Locate the cells, classifying each as a parasitized red blood cell, an uninfected red blood cell, or a white blood cell.
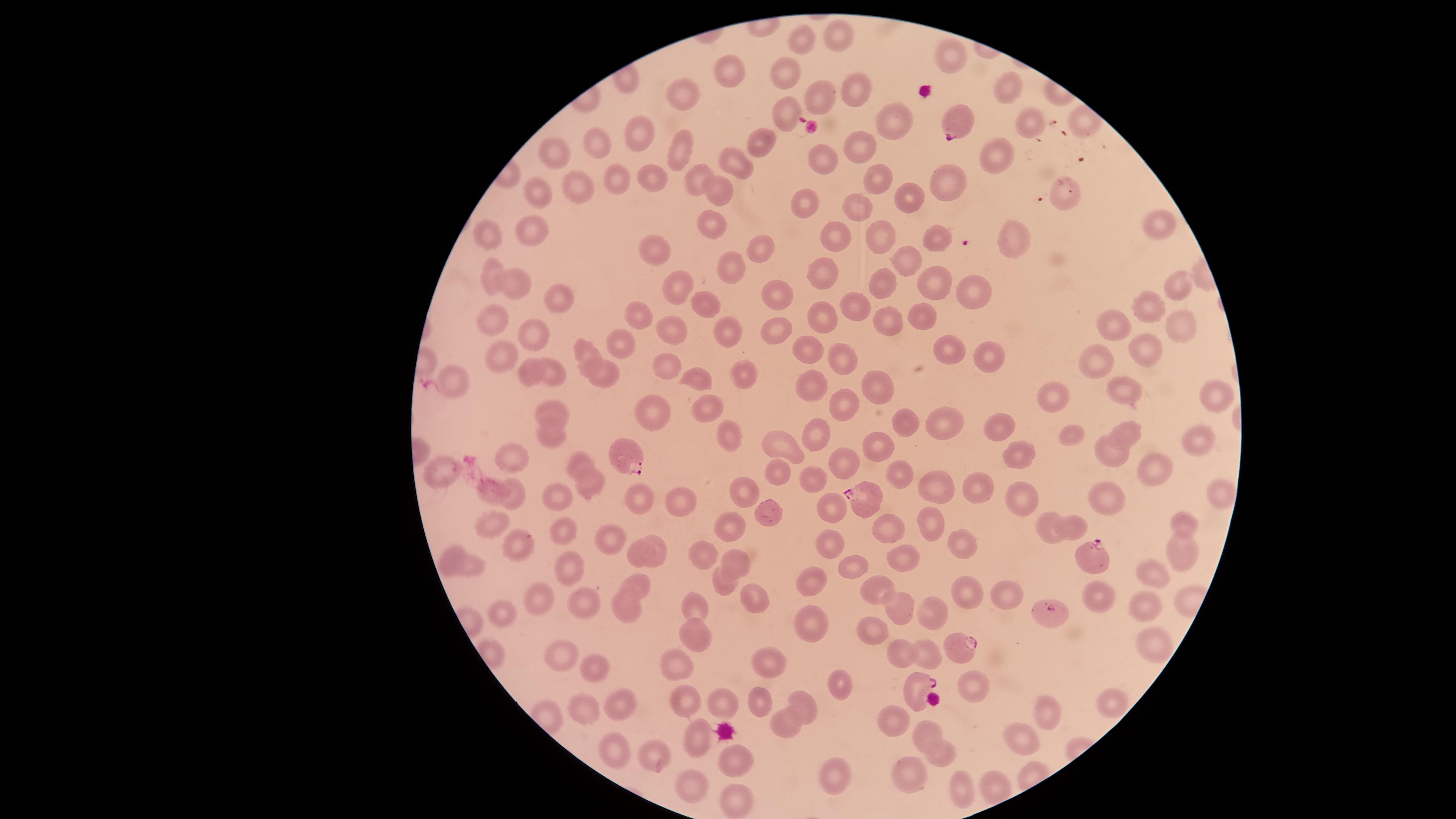

Approximate marker points as {x, y} in pixels.
Parasitized red blood cells: {958, 129}, {627, 462}, {861, 496}, {1087, 562}, {1051, 614}, {948, 649}, {912, 693}.
Uninfected red blood cells: {838, 31}, {805, 42}, {733, 69}, {789, 70}, {850, 85}, {1009, 87}, {679, 91}, {817, 97}, {781, 108}, {1027, 119}, {892, 123}, {639, 135}, {760, 138}, {600, 144}, {862, 146}, {995, 149}, {823, 153}, {683, 154}, {555, 157}, {740, 157}, {698, 176}, {877, 178}, {653, 179}, {620, 180}, {951, 184}, {581, 188}, {536, 190}, {1064, 196}, {721, 197}, {804, 198}, {911, 200}, {858, 209}, {711, 219}, {1156, 227}, {539, 228}, {838, 233}, {481, 234}, {877, 235}, {937, 240}, {1015, 242}, {658, 245}, {761, 247}, {903, 266}, {728, 268}, {488, 271}, {820, 271}, {875, 278}, {516, 282}, {932, 282}, {1175, 284}, {682, 286}, {775, 291}, {972, 295}, {550, 297}, {702, 306}, {858, 309}, {1146, 309}, {639, 314}, {923, 318}, {819, 320}, {887, 322}, {493, 323}, {1115, 326}, {770, 328}, {1181, 329}, {672, 331}, {727, 332}, {530, 333}, {617, 339}, {582, 351}, {1139, 351}, {942, 352}, {803, 353}, {986, 355}, {504, 356}, {837, 358}, {1091, 360}, {669, 363}, {528, 372}, {551, 374}, {747, 374}, {602, 375}, {695, 382}, {456, 385}, {874, 386}, {1123, 390}, {815, 393}, {1051, 396}, {1205, 396}, {844, 407}, {654, 411}, {703, 412}, {549, 413}, {911, 421}, {943, 425}, {1003, 426}, {816, 430}, {1071, 432}, {1132, 432}, {553, 438}, {734, 438}, {1198, 443}, {873, 445}, {790, 448}, {1019, 449}, {1113, 451}, {512, 452}, {582, 456}, {844, 463}, {903, 469}, {1156, 470}, {441, 473}, {778, 474}, {978, 481}, {587, 482}, {935, 484}, {814, 485}, {486, 488}, {1221, 489}, {1020, 497}, {509, 498}, {561, 498}, {640, 498}, {680, 499}, {746, 499}, {1107, 500}, {829, 511}, {770, 512}, {1179, 522}, {929, 524}, {498, 525}, {1073, 525}, {561, 527}, {735, 528}, {1043, 528}, {888, 531}, {607, 535}, {655, 538}, {959, 541}, {827, 545}, {1179, 546}, {515, 547}, {449, 550}, {637, 552}, {906, 553}, {704, 555}, {733, 559}, {468, 566}, {570, 567}, {853, 570}, {1151, 574}, {726, 578}, {807, 582}, {640, 585}, {880, 588}, {1002, 590}, {965, 591}, {752, 593}, {1105, 594}, {580, 596}, {692, 606}, {1148, 607}, {628, 608}, {895, 608}, {933, 611}, {503, 612}, {809, 618}, {873, 628}, {695, 636}, {1150, 645}, {897, 650}, {926, 651}, {560, 656}, {767, 658}, {678, 662}, {597, 668}, {839, 682}, {975, 688}, {758, 697}, {1102, 698}, {685, 699}, {726, 699}, {619, 706}, {806, 706}, {583, 711}, {1043, 713}, {898, 717}, {787, 725}, {926, 730}, {696, 737}, {1022, 740}, {615, 753}, {651, 753}, {940, 755}, {735, 762}, {911, 774}, {829, 778}, {687, 780}, {962, 787}, {731, 803}.
No white blood cells identified.

capture = smartphone photograph through the microscope eyepiece
field of view = single
visible region = circular
image size = 1456×819 pixels
stain = Giemsa
preparation = thin smear of blood
species = Plasmodium falciparum